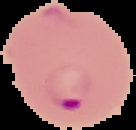

result = malaria parasites detected
preparation = thin blood smear
image type = segmented cell region on a black background
image size = 136×130 pixels